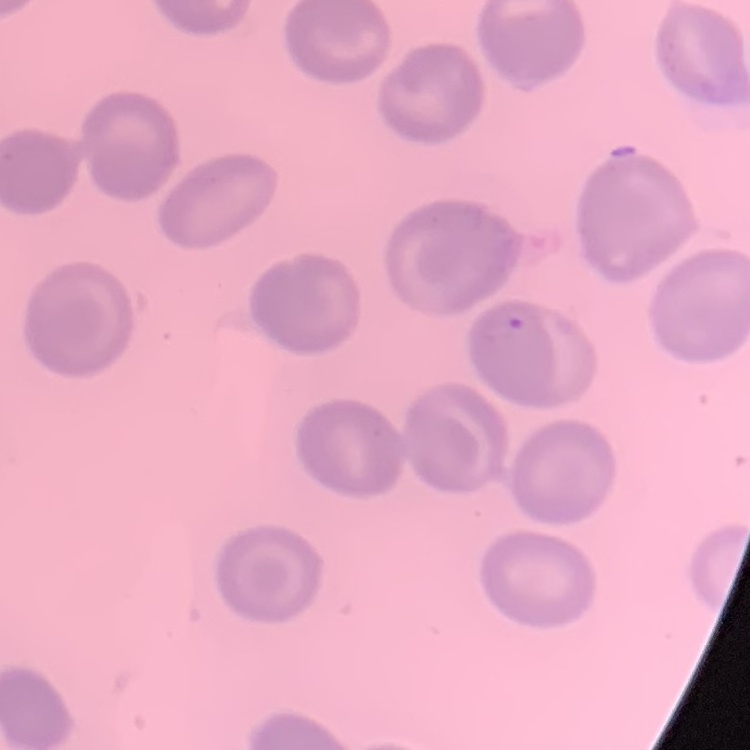 The red blood cells show no rouleaux formation. Thin peripheral smear. Field's or Giemsa stain. Square crop of a larger photomicrograph.